Identify the blood parasite species.
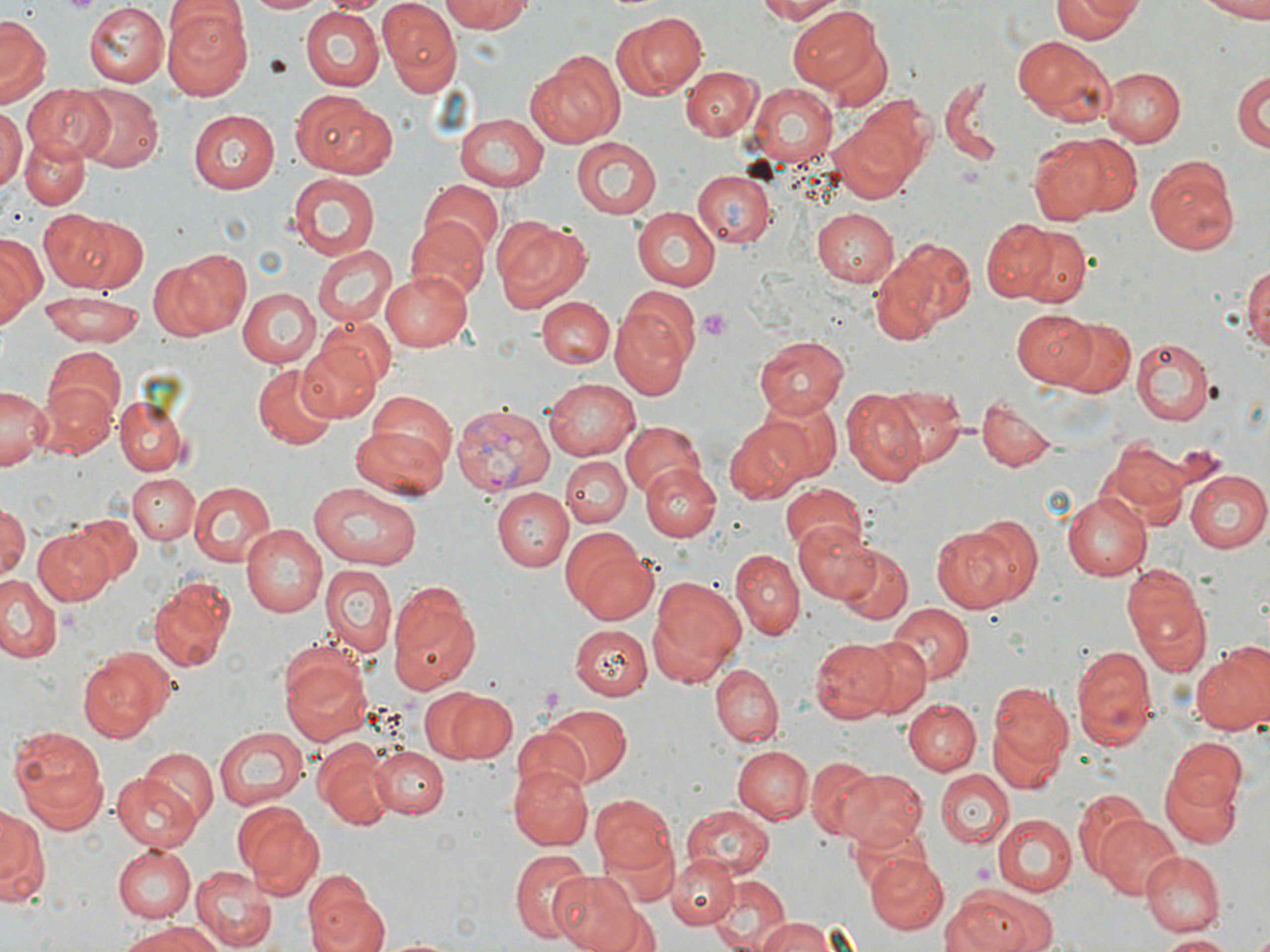
Plasmodium vivax.

preparation = thin blood film
modality = optical microscopy
Plasmodium vivax-infected red blood cell locations = approximate bounding boxes as [x1, y1, x2, y2] in pixels: [452, 402, 555, 495]
magnification = 1000x
uninfected red blood cell locations = approximate bounding boxes as [x1, y1, x2, y2] in pixels: [243, 0, 328, 15], [322, 0, 391, 16], [442, 0, 533, 33], [753, 0, 847, 24], [1054, 0, 1141, 42], [1187, 0, 1270, 19], [378, 2, 464, 97], [84, 4, 169, 86], [163, 5, 253, 102], [788, 7, 884, 91], [297, 9, 383, 91], [611, 13, 706, 98], [0, 18, 48, 105], [1012, 36, 1116, 126], [529, 51, 624, 146], [680, 65, 762, 140], [1233, 65, 1269, 154], [1101, 66, 1187, 145], [939, 77, 1008, 169], [746, 82, 841, 166], [24, 84, 116, 163], [76, 88, 162, 173], [291, 92, 397, 179], [854, 95, 937, 182], [0, 108, 24, 192], [188, 110, 278, 193], [454, 112, 550, 188], [832, 118, 921, 201], [19, 134, 90, 210], [1028, 135, 1115, 226], [1063, 135, 1143, 216], [572, 137, 662, 219], [1145, 153, 1243, 253], [290, 171, 379, 259], [693, 171, 776, 248], [682, 180, 844, 259], [419, 181, 503, 260], [631, 207, 719, 290], [812, 207, 901, 285], [41, 208, 125, 291], [79, 217, 147, 295], [406, 217, 489, 302], [494, 218, 591, 313], [982, 222, 1053, 302], [1016, 227, 1090, 304], [0, 234, 43, 325], [877, 240, 974, 335], [310, 244, 396, 328], [158, 249, 248, 338], [1242, 261, 1270, 361], [379, 269, 471, 351], [236, 287, 320, 368], [34, 290, 149, 347], [537, 297, 613, 369], [612, 303, 692, 399], [1011, 308, 1097, 386], [1047, 316, 1135, 399], [317, 317, 395, 387], [755, 336, 848, 418], [1129, 337, 1215, 426], [298, 340, 385, 422], [43, 347, 126, 432], [253, 364, 336, 450], [545, 377, 638, 463], [33, 379, 118, 461], [0, 383, 47, 468], [876, 384, 968, 468], [363, 390, 458, 481], [843, 390, 927, 487], [754, 393, 841, 483], [114, 394, 188, 474], [976, 398, 1057, 473], [621, 421, 705, 497], [724, 422, 810, 504], [352, 425, 449, 501], [1104, 437, 1192, 524], [561, 454, 630, 526], [641, 464, 720, 541], [1185, 471, 1270, 553], [127, 473, 200, 547], [186, 480, 276, 567], [779, 481, 864, 553], [309, 483, 422, 569], [492, 488, 572, 572], [1060, 490, 1151, 583], [0, 502, 28, 585], [71, 514, 140, 582], [964, 515, 1045, 605], [793, 520, 882, 602], [241, 524, 326, 616], [931, 526, 1023, 612], [32, 529, 114, 606], [563, 535, 658, 625], [838, 545, 912, 624], [730, 549, 803, 640], [319, 563, 397, 662], [1120, 564, 1213, 679], [0, 575, 65, 665], [645, 575, 746, 686], [148, 576, 235, 671], [386, 580, 481, 696], [887, 604, 972, 684], [568, 624, 652, 699], [811, 638, 893, 723], [856, 638, 927, 715], [1070, 645, 1158, 752], [1192, 648, 1270, 739], [76, 650, 172, 744], [280, 650, 371, 745], [713, 664, 782, 746], [429, 685, 515, 764], [984, 687, 1072, 789], [896, 699, 998, 834], [903, 700, 980, 774], [539, 705, 632, 787], [7, 726, 110, 833], [212, 727, 307, 811], [509, 727, 589, 804], [1165, 738, 1247, 813], [313, 743, 390, 830], [372, 745, 450, 820], [732, 746, 811, 823], [140, 748, 220, 830], [807, 757, 882, 837], [508, 763, 593, 850], [1158, 764, 1243, 848], [836, 768, 926, 851], [934, 770, 1014, 848], [111, 772, 205, 852], [1073, 789, 1155, 882], [591, 793, 680, 881], [231, 799, 322, 897], [0, 806, 45, 906], [681, 806, 775, 880], [1095, 813, 1183, 898], [994, 814, 1076, 897], [678, 832, 773, 946], [111, 843, 196, 923], [509, 849, 593, 941], [1139, 851, 1224, 937], [667, 854, 739, 930], [866, 854, 948, 935], [192, 864, 279, 950], [301, 869, 386, 952], [549, 870, 646, 951], [711, 875, 791, 952], [952, 885, 1054, 952], [753, 915, 839, 952], [123, 921, 224, 952], [1157, 933, 1241, 950]
image size = 1270×952 pixels
stain = May-Grünwald-Giemsa
field of view = single
platelet locations = approximate bounding boxes as [x1, y1, x2, y2] in pixels: [59, 0, 100, 17], [697, 307, 733, 340], [536, 685, 570, 718]